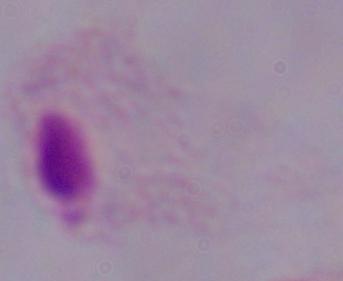

Summary:
  - Magnification: 1000x
  - Identification: trichomonad
  - Modality: photomicrograph